Name the parasite shown.
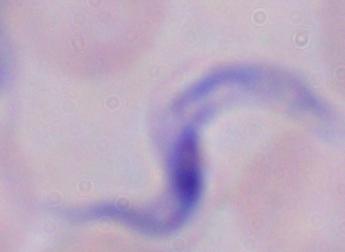
A trypanosome.

magnification = 1000x
modality = photomicrograph